Describe the morphology of the red blood cells.
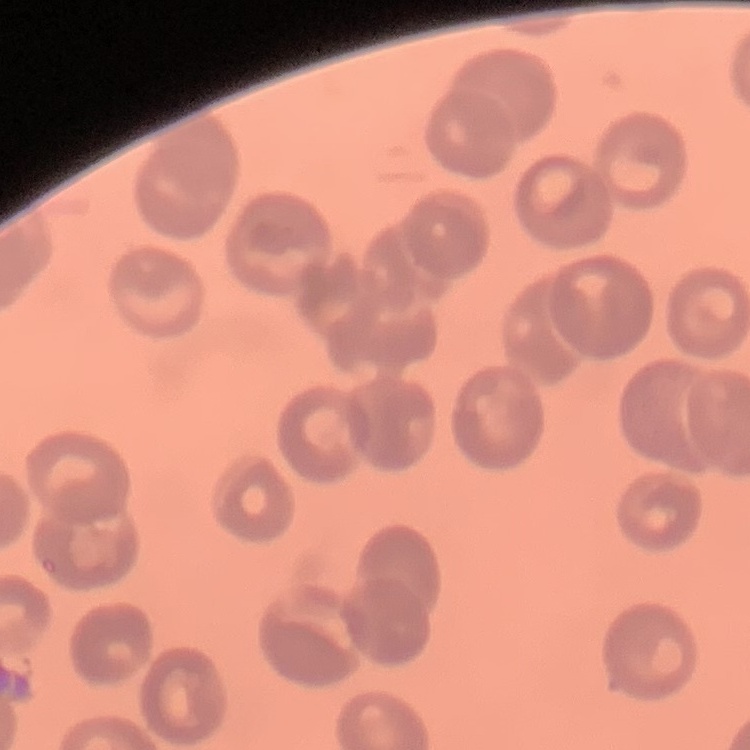

No rouleaux formation.

Summary:
  - Preparation: thin blood film
  - Image type: square crop of a larger photomicrograph
  - Stain: Field's or Giemsa